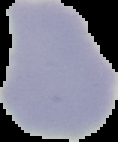 Image is 118×142 pixels. From a thin blood film. The area outside the segmented cell region is set to black. Result: no malaria parasites seen.